Assess this cell for malaria.
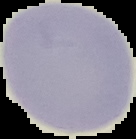

Uninfected.

{
  "preparation": "thin blood smear",
  "image_size": "136×139 pixels",
  "image_type": "segmented cell region on a black background"
}